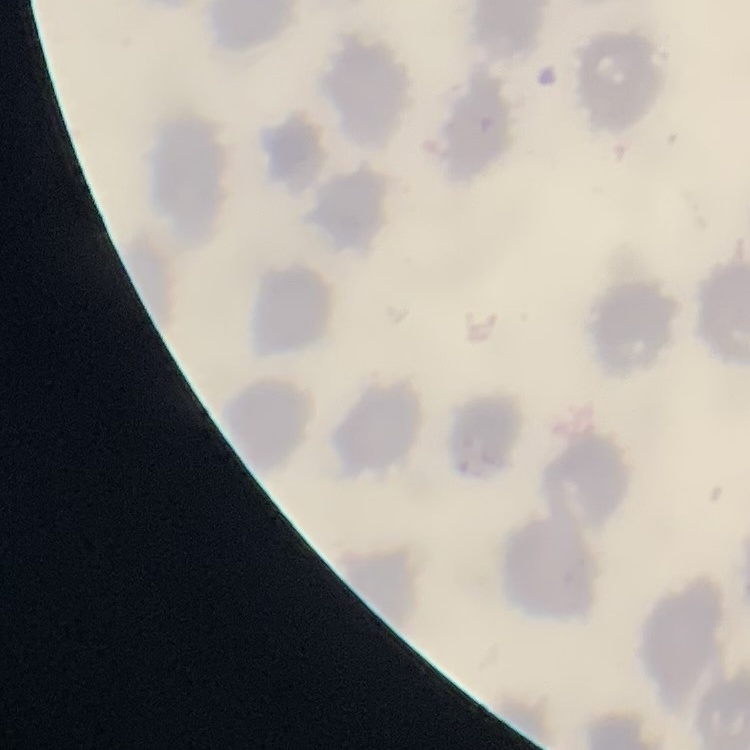
Summary:
  - Erythrocyte morphology: no rouleaux formation
  - Image type: one tile cut from a larger photomicrograph
  - Stain: Field's or Giemsa
  - Preparation: thin peripheral smear